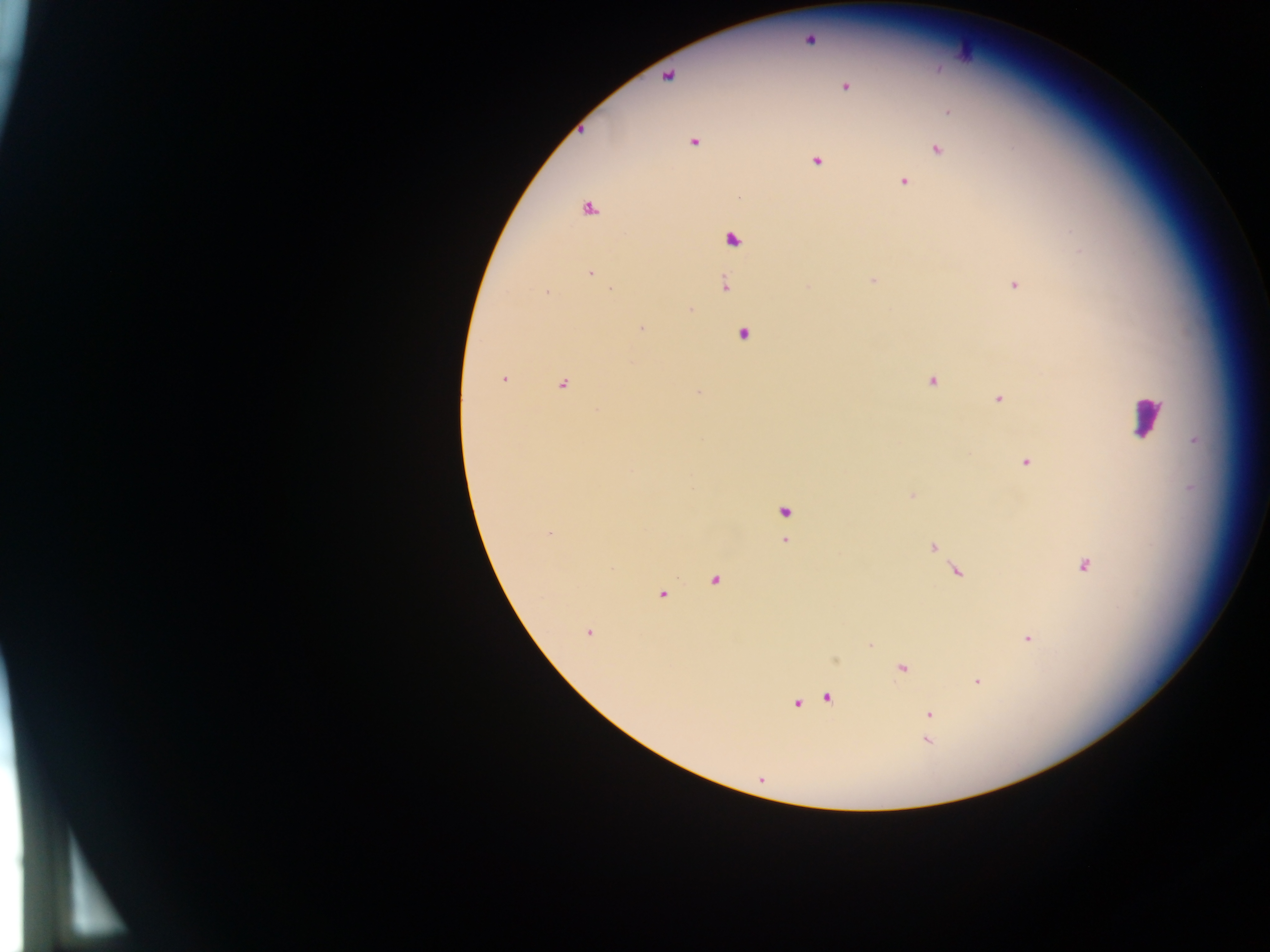

field of view = single
country = Ghana
image size = 1270×952 pixels
leukocyte locations = approximate centers as x y in pixels: 1146 417
malaria parasite locations = approximate centers as x y in pixels: 809 40; 668 76; 845 87; 948 112; 694 142; 937 150; 816 161; 904 182; 588 210; 733 239; 590 273; 872 280; 725 285; 1015 285; 807 286; 611 289; 547 292; 690 309; 641 328; 744 333; 503 379; 932 381; 562 384; 698 392; 999 398; 1026 462; 912 495; 784 513; 549 532; 785 541; 932 547; 1083 565; 956 571; 714 582; 662 595; 588 632; 1028 638; 902 668; 977 682; 828 698; 797 703; 930 714; 926 741
capture = mobile-phone photograph through a microscope
preparation = thick blood smear